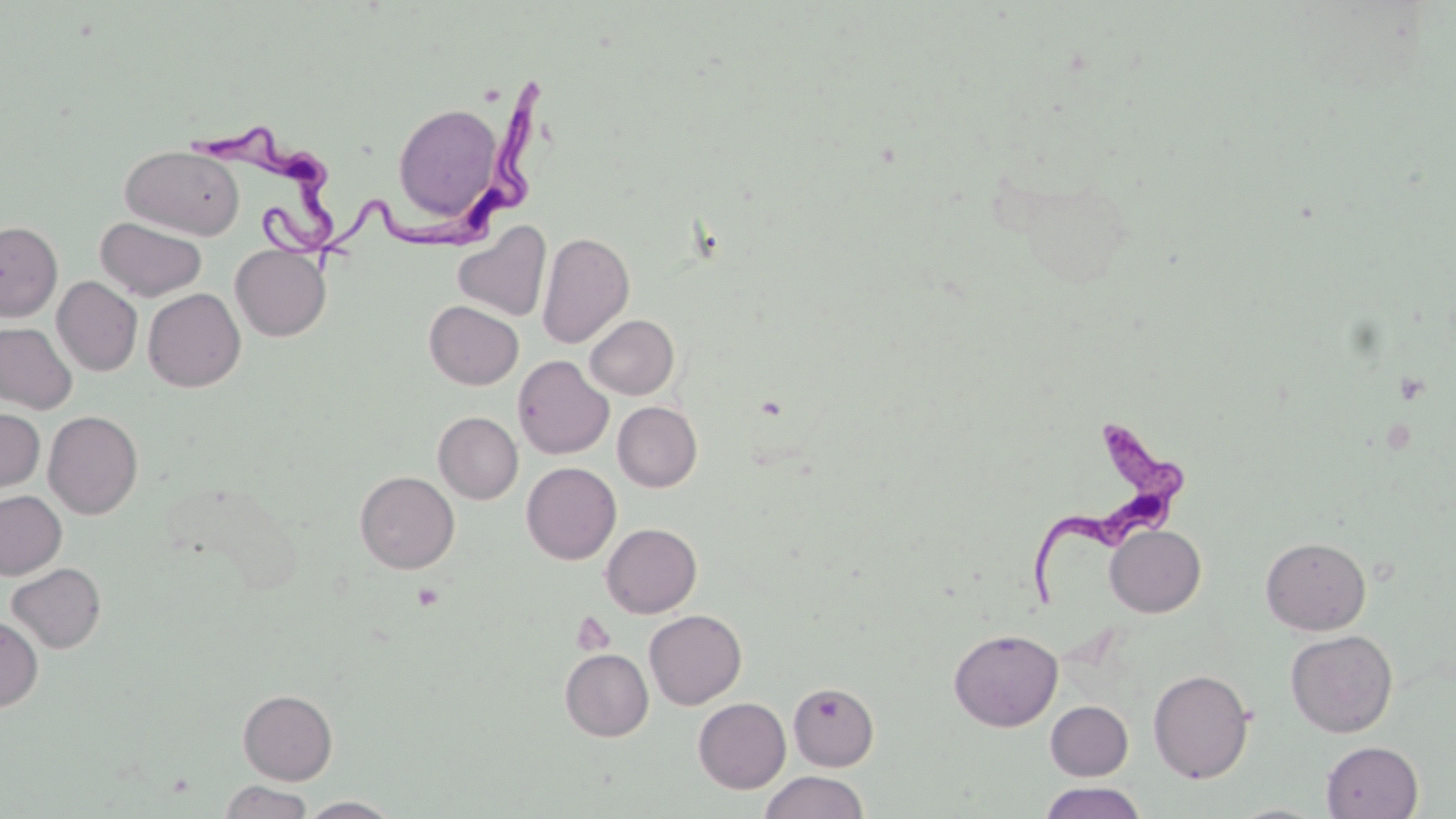

slide-level diagnosis = Trypanosoma brucei
magnification = 1000x
stain = May-Grünwald-Giemsa
modality = light microscopy
Trypanosoma brucei locations = approximate bounding boxes as [x1, y1, x2, y2] in pixels: [324, 74, 560, 270], [194, 120, 347, 254], [1023, 418, 1189, 604]
field of view = one of a larger specimen
platelet locations = approximate bounding boxes as [x1, y1, x2, y2] in pixels: [411, 582, 445, 610], [572, 612, 616, 656]
uninfected red blood cell locations = approximate bounding boxes as [x1, y1, x2, y2] in pixels: [392, 101, 505, 225], [121, 144, 245, 240], [95, 216, 207, 302], [0, 221, 63, 321], [452, 221, 551, 322], [536, 231, 635, 348], [230, 244, 331, 341], [52, 276, 142, 376], [143, 289, 246, 392], [425, 300, 524, 389], [584, 314, 678, 399], [0, 321, 77, 414], [513, 355, 614, 459], [612, 401, 702, 491], [0, 408, 44, 494], [43, 410, 144, 519], [433, 411, 523, 504], [521, 462, 621, 564], [354, 471, 459, 574], [0, 490, 66, 579], [601, 523, 702, 618], [1105, 525, 1206, 617], [1260, 536, 1371, 635], [6, 562, 106, 653], [644, 609, 747, 709], [0, 615, 43, 712], [949, 629, 1062, 731], [1285, 630, 1398, 737], [560, 648, 653, 741], [1148, 668, 1254, 783], [788, 681, 879, 771], [238, 689, 337, 785], [693, 697, 791, 793], [1046, 701, 1133, 780], [1321, 741, 1423, 818], [760, 771, 869, 819], [219, 780, 313, 819], [1037, 782, 1148, 819], [299, 797, 402, 818]
preparation = thin blood film
image size = 1456×819 pixels